Name the parasite shown.
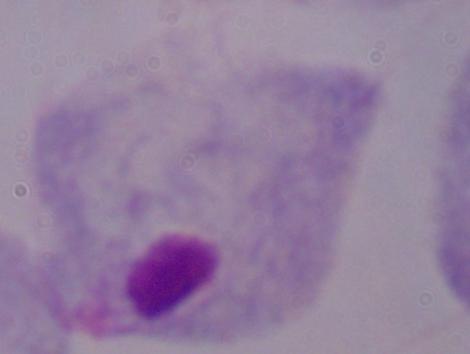

A trichomonad.

Micrograph. Captured at 1000x magnification.